Classify this cell by malaria status.
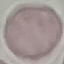
It is uninfected.

{
  "image_type": "cell patch, automatically extracted from a larger field of view and resized to 64 × 64 pixels",
  "capture": "smartphone through the microscope eyepiece",
  "stain": "Giemsa",
  "preparation": "thin smear"
}